Locate every blood parasite and identify its species.
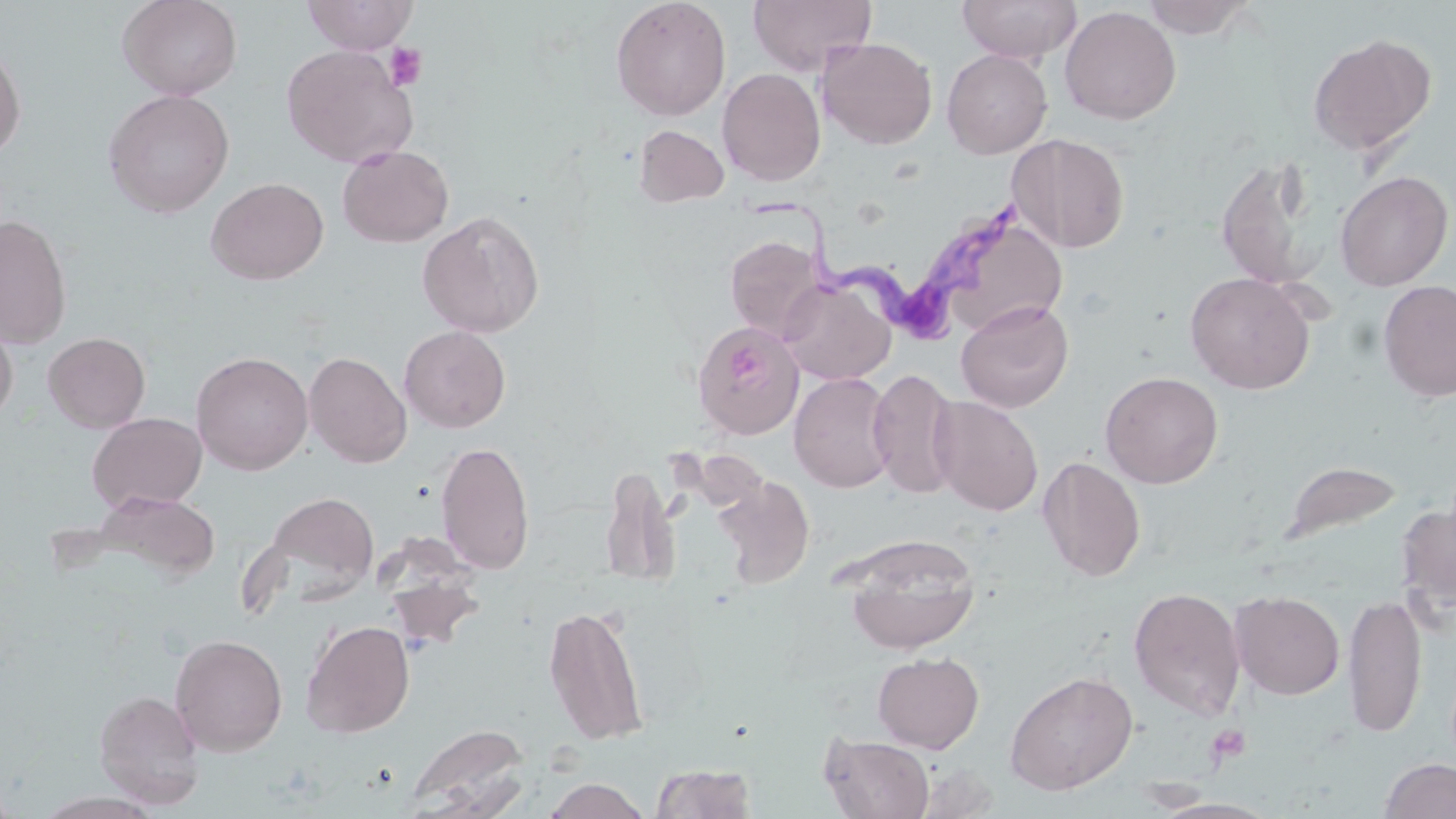

Approximate bounding boxes as (x1,y1)-(x2,y2) corner pairs in pixels.
Trypanosoma brucei: (749,198)-(1023,328).
No Plasmodium falciparum, Plasmodium ovale, Plasmodium malariae, Plasmodium vivax, or Babesia divergens observed.

Summary:
  - Uninfected red blood cell locations: (117,0)-(242,100), (302,0)-(418,54), (610,0)-(731,120), (748,0)-(876,76), (958,0)-(1080,63), (1139,0)-(1257,39), (1060,5)-(1181,125), (1307,32)-(1436,157), (817,37)-(937,149), (0,41)-(26,161), (280,44)-(418,168), (942,49)-(1052,158), (717,68)-(826,186), (102,88)-(234,217), (633,124)-(730,208), (1007,133)-(1130,253), (337,144)-(454,247), (1216,156)-(1326,291), (1335,170)-(1453,291), (206,177)-(329,285), (941,206)-(1067,340), (417,210)-(545,337), (1,213)-(72,349), (725,235)-(825,342), (1184,271)-(1316,394), (779,277)-(895,385), (1378,280)-(1456,402), (955,300)-(1074,413), (0,314)-(18,427), (693,320)-(805,439), (399,325)-(511,433), (43,332)-(150,433), (191,351)-(313,475), (304,351)-(411,468), (868,368)-(962,498), (789,371)-(898,493), (1100,371)-(1224,488), (930,396)-(1044,516), (88,412)-(207,513), (436,439)-(535,575), (1038,456)-(1146,581), (1283,460)-(1403,545), (600,466)-(681,587), (713,474)-(815,588), (90,489)-(222,584), (263,491)-(380,598), (1395,504)-(1456,618), (844,536)-(979,653), (1128,586)-(1247,720), (1230,590)-(1345,700), (1343,591)-(1427,739), (544,601)-(649,745), (301,620)-(415,738), (169,633)-(288,756), (872,652)-(984,753), (1005,670)-(1139,795), (94,689)-(205,809), (404,723)-(531,817), (820,733)-(935,818), (1379,758)-(1456,818), (649,762)-(758,818), (914,762)-(1000,819), (543,778)-(651,819)
  - Platelet locations: (384,43)-(427,91), (725,344)-(776,392), (1205,724)-(1252,766)
  - Slide-level diagnosis: Trypanosoma brucei
  - Magnification: 1000x
  - Field of view: single
  - Modality: light microscopy
  - Image size: 1456×819 pixels
  - Stain: May-Grünwald-Giemsa
  - Preparation: thin blood smear